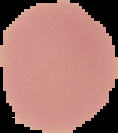
{
  "image_size": "118×133 pixels",
  "preparation": "thin blood film",
  "result": "no malaria parasites seen",
  "image_type": "cell region segmented out of the field of view; surrounding area masked to black"
}